Locate every leukocyte (white blood cell).
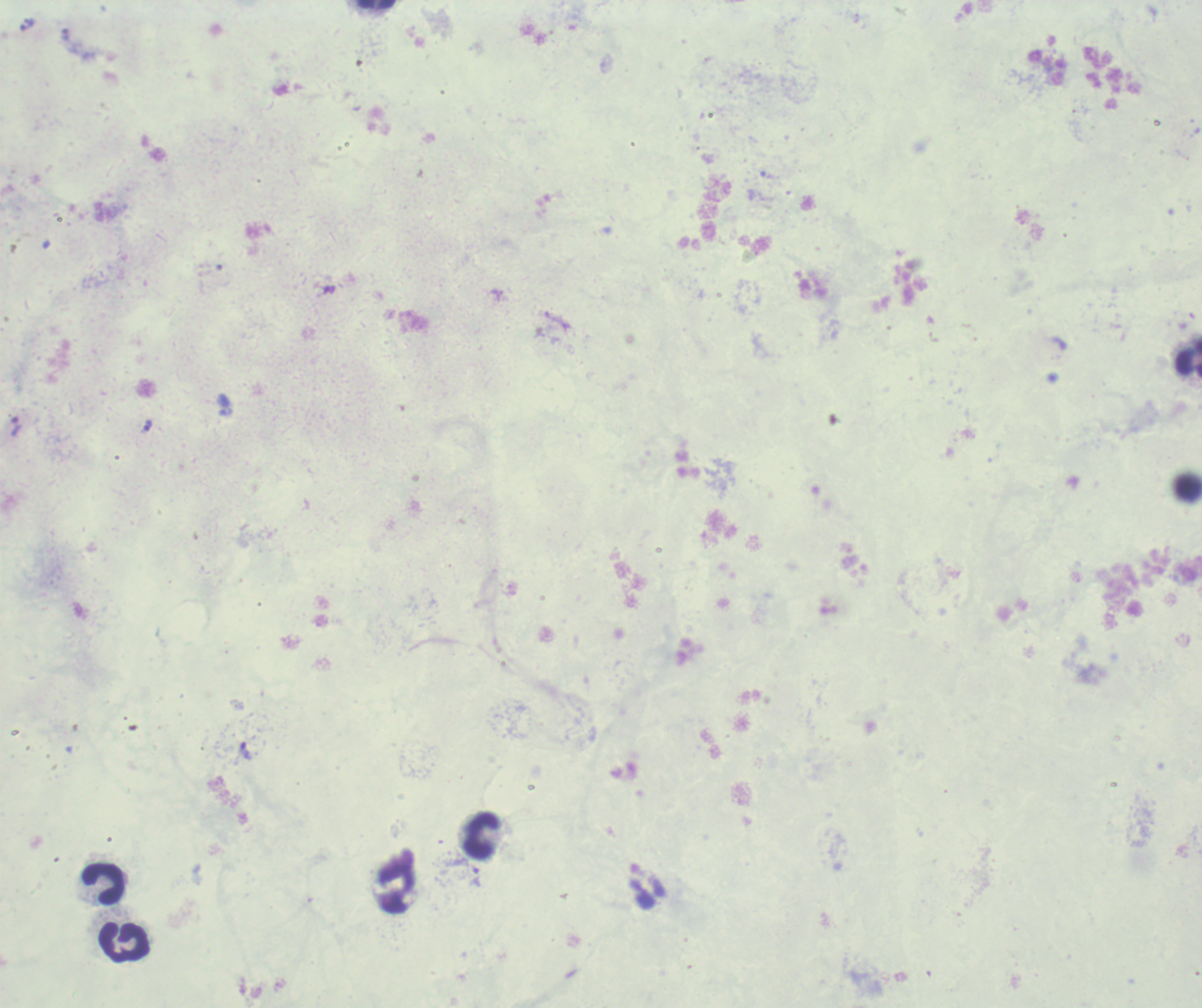

Approximate centers as [x, y] in pixels.
Leukocytes: [376, 4], [1188, 358], [481, 834], [103, 884], [124, 941].

{
  "field_of_view": "one from this slide",
  "result": "malaria parasites detected",
  "magnification": "100x",
  "stain": "Romanowsky",
  "background_quality": "poor",
  "trophozoite_locations": "approximate centers as [x, y] in pixels: [244, 750], [474, 876]",
  "image_size": "1202×1008 pixels",
  "context": "previously used in a real diagnosis",
  "preparation": "thick blood smear"
}